Identify the parasite.
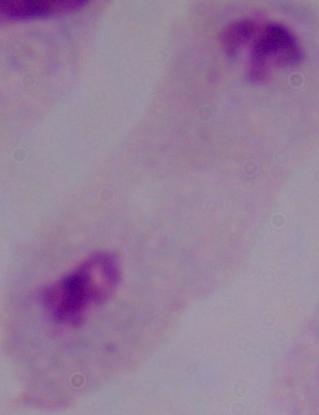

This is a trichomonad.

modality = micrograph
magnification = 1000x